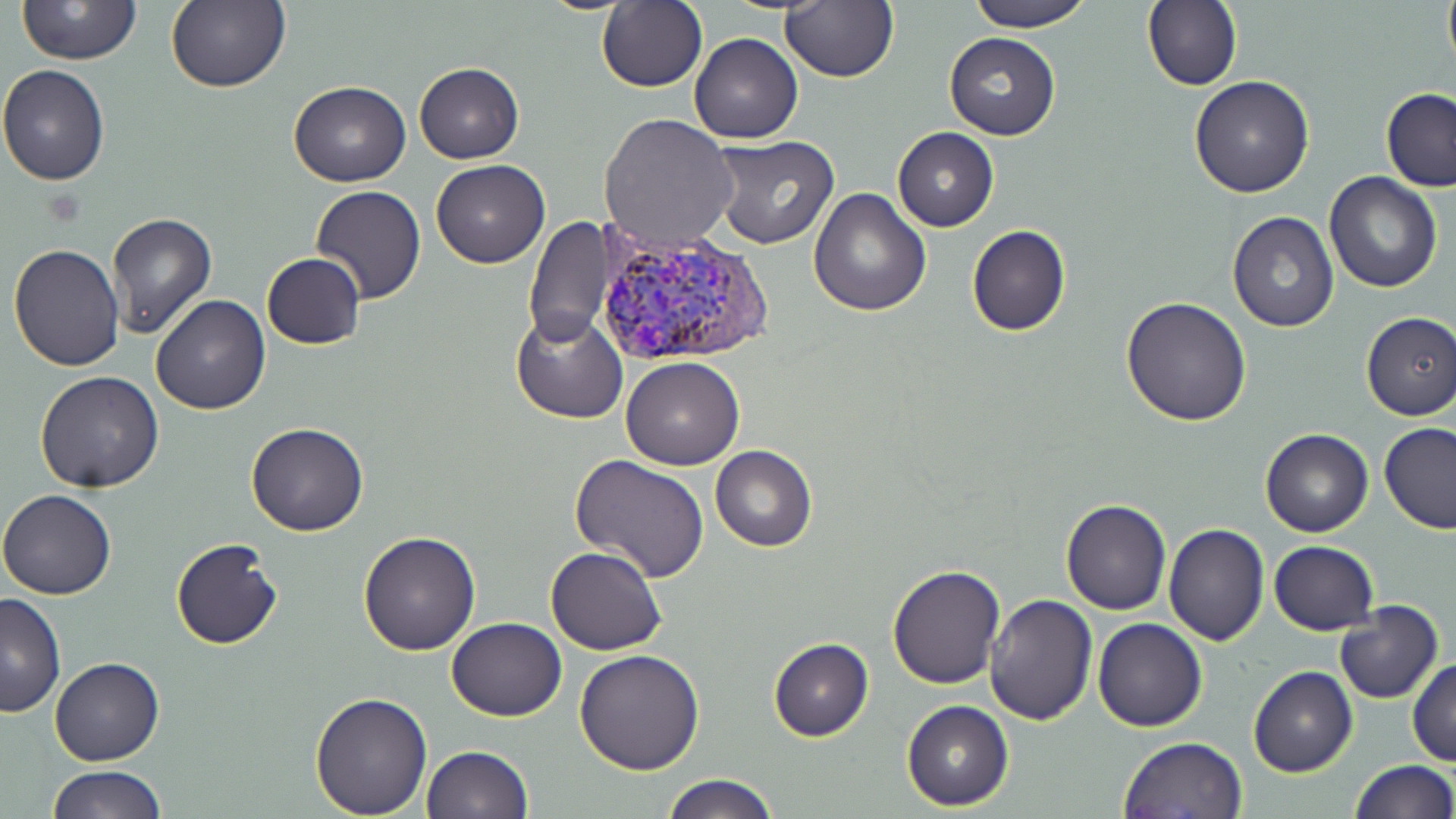
Approximate bounding boxes as named x1/y1/x2/y2 corners in pixels. Plasmodium vivax-infected red blood cell locations: (x1=594, y1=228, x2=777, y2=369). Uninfected red blood cell locations: (x1=596, y1=0, x2=706, y2=92), (x1=780, y1=0, x2=899, y2=84), (x1=963, y1=0, x2=1096, y2=32), (x1=1142, y1=0, x2=1242, y2=91), (x1=1442, y1=0, x2=1455, y2=73), (x1=16, y1=1, x2=143, y2=65), (x1=167, y1=1, x2=290, y2=94), (x1=944, y1=31, x2=1060, y2=141), (x1=690, y1=32, x2=803, y2=144), (x1=413, y1=62, x2=524, y2=163), (x1=0, y1=63, x2=112, y2=184), (x1=1188, y1=75, x2=1314, y2=197), (x1=288, y1=79, x2=410, y2=186), (x1=1380, y1=88, x2=1456, y2=192), (x1=599, y1=112, x2=736, y2=251), (x1=892, y1=128, x2=998, y2=232), (x1=708, y1=134, x2=839, y2=249), (x1=431, y1=159, x2=550, y2=268), (x1=1323, y1=170, x2=1443, y2=293), (x1=311, y1=185, x2=426, y2=304), (x1=808, y1=186, x2=931, y2=316), (x1=107, y1=211, x2=217, y2=338), (x1=1227, y1=211, x2=1339, y2=332), (x1=524, y1=217, x2=613, y2=350), (x1=967, y1=224, x2=1071, y2=337), (x1=8, y1=244, x2=125, y2=371), (x1=261, y1=253, x2=366, y2=348), (x1=150, y1=294, x2=271, y2=414), (x1=1122, y1=295, x2=1253, y2=426), (x1=510, y1=308, x2=629, y2=423), (x1=1360, y1=311, x2=1456, y2=421), (x1=622, y1=357, x2=744, y2=470), (x1=36, y1=372, x2=165, y2=492), (x1=245, y1=422, x2=369, y2=537), (x1=1379, y1=422, x2=1455, y2=533), (x1=1261, y1=428, x2=1373, y2=538), (x1=710, y1=445, x2=816, y2=551), (x1=570, y1=454, x2=711, y2=583), (x1=0, y1=489, x2=118, y2=599), (x1=1059, y1=498, x2=1171, y2=616), (x1=1163, y1=524, x2=1269, y2=645), (x1=359, y1=531, x2=480, y2=656), (x1=170, y1=537, x2=283, y2=649), (x1=1269, y1=541, x2=1379, y2=634), (x1=545, y1=546, x2=667, y2=655), (x1=887, y1=563, x2=1006, y2=689), (x1=986, y1=592, x2=1098, y2=724), (x1=0, y1=594, x2=65, y2=718), (x1=1334, y1=601, x2=1443, y2=705), (x1=446, y1=617, x2=567, y2=720), (x1=1093, y1=618, x2=1207, y2=731), (x1=767, y1=638, x2=874, y2=742), (x1=575, y1=648, x2=706, y2=774), (x1=49, y1=657, x2=163, y2=766), (x1=1408, y1=658, x2=1456, y2=766), (x1=1249, y1=667, x2=1358, y2=778), (x1=310, y1=690, x2=432, y2=818), (x1=901, y1=700, x2=1013, y2=811), (x1=1118, y1=735, x2=1247, y2=818), (x1=421, y1=745, x2=533, y2=818), (x1=1348, y1=759, x2=1455, y2=818), (x1=46, y1=765, x2=166, y2=819), (x1=660, y1=774, x2=778, y2=818). Slide-level diagnosis: Plasmodium vivax. May-Grünwald-Giemsa stain. Image is 1456×819 pixels. Thin blood film. Captured at 1000x magnification. Light microscopy. One field of a larger specimen.